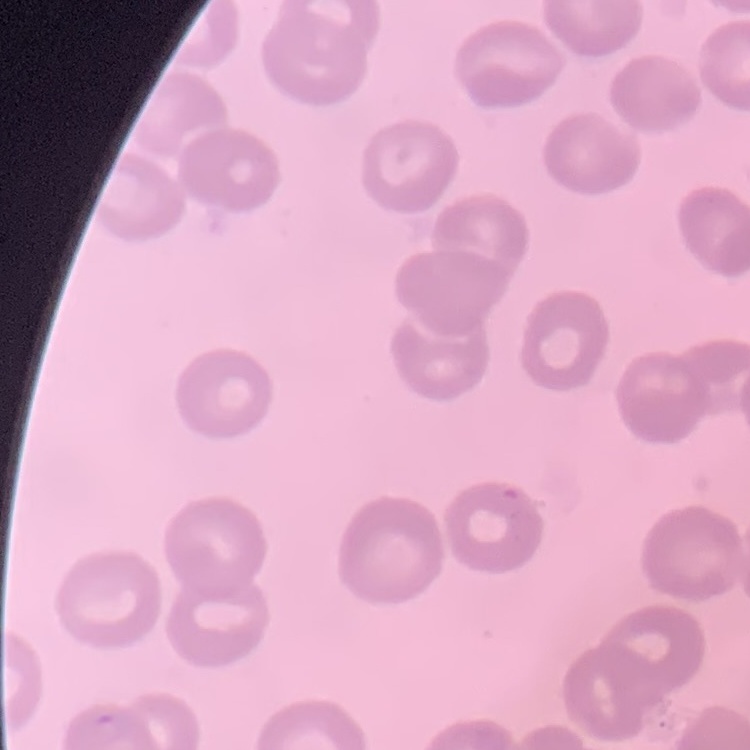
Summary:
  - Red blood cell morphology: no rouleaux formation
  - Preparation: thin blood smear
  - Stain: Field's or Giemsa
  - Image type: square crop of a larger photomicrograph